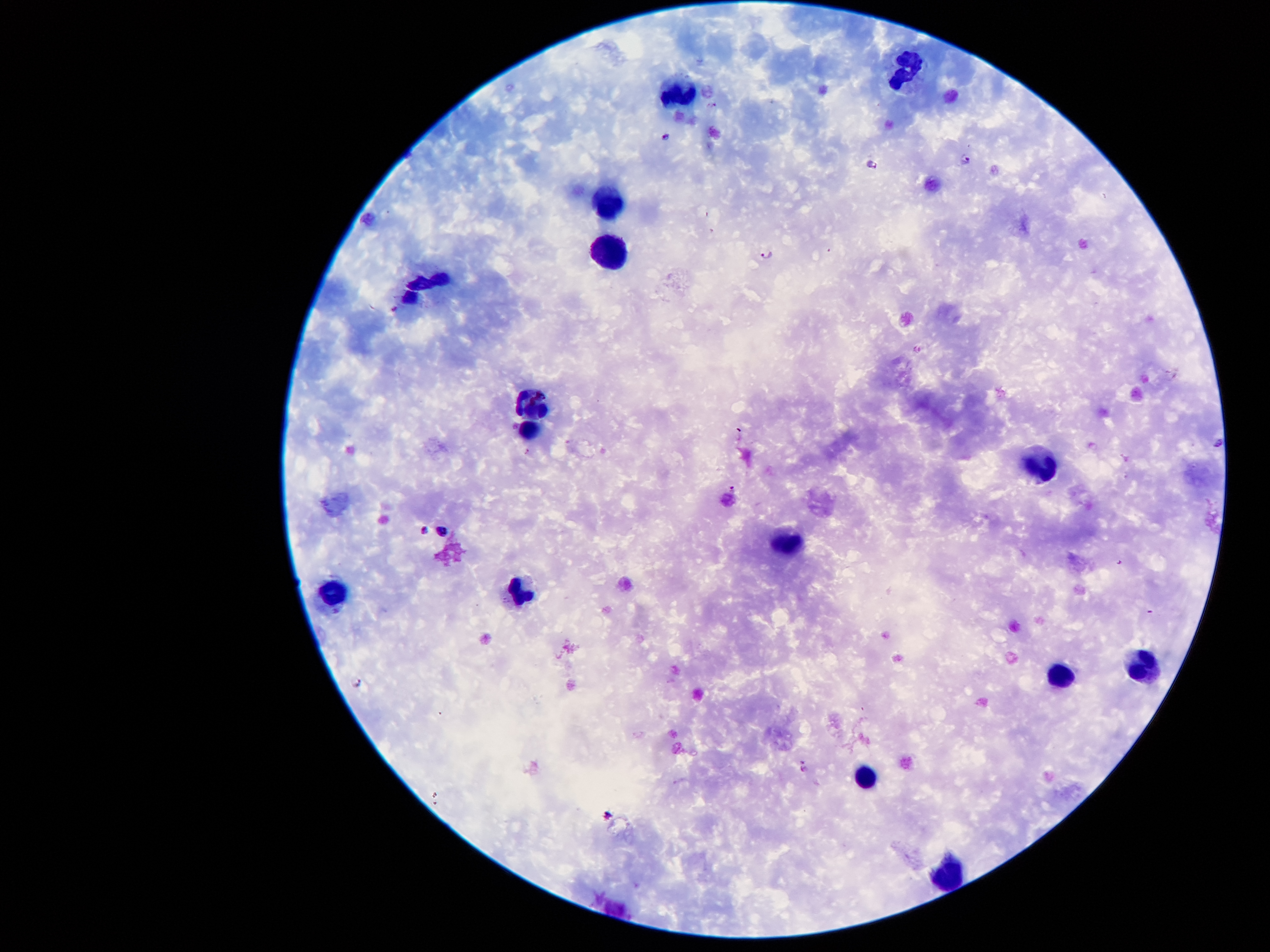
Approximate centers as {x, y} in pixels.
Summary:
  - Leukocyte locations: {909, 71}, {679, 90}, {608, 200}, {613, 253}, {422, 284}, {526, 405}, {530, 429}, {1039, 465}, {786, 542}, {333, 592}, {521, 592}, {1140, 672}, {1056, 676}, {865, 778}, {951, 873}
  - Malaria parasite locations: {668, 139}, {968, 159}, {870, 167}, {769, 255}, {1220, 442}, {733, 488}, {422, 530}, {444, 530}, {357, 684}, {806, 766}, {606, 815}
  - Magnification: 100x
  - Stain: Giemsa
  - Field of view: single
  - Patient malaria status: infected with Plasmodium falciparum
  - Capture: smartphone through the microscope eyepiece
  - Preparation: thick blood smear
  - Image size: 1270×952 pixels